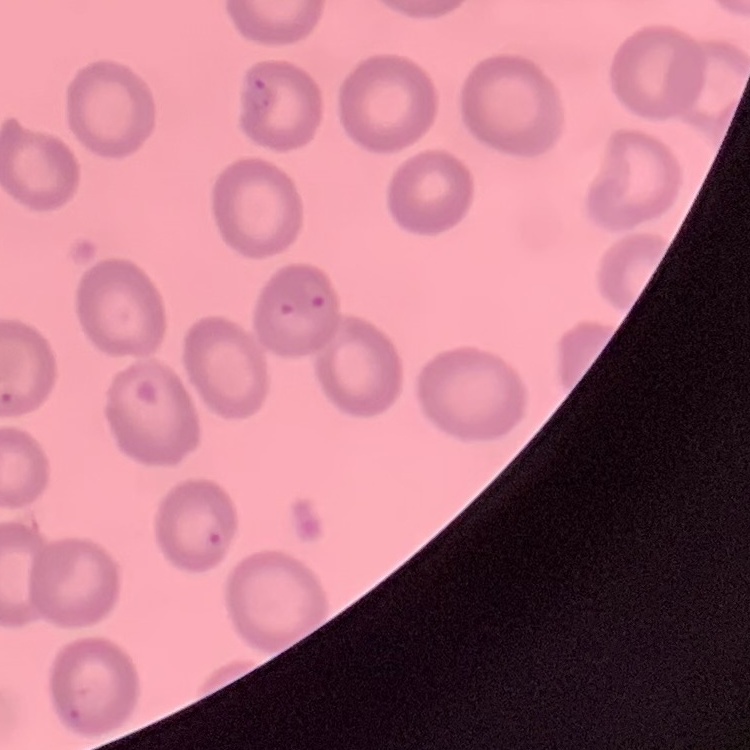

The red blood cells exhibit no rouleaux formation. Field's or Giemsa stain. One tile cut from a larger photomicrograph. Thin blood film.